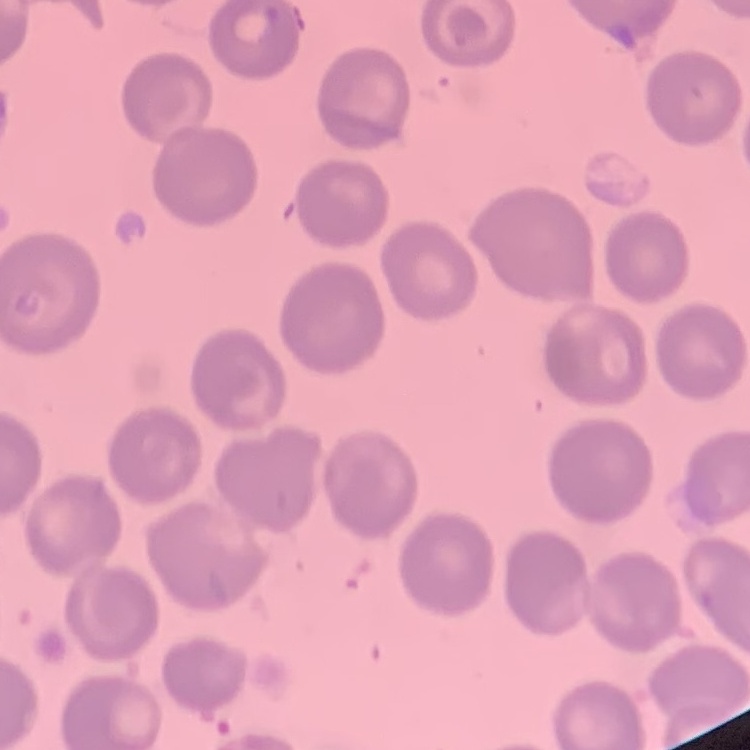
The erythrocytes show no rouleaux formation. Field's or Giemsa stain. One tile cut from a larger photomicrograph. Thin blood smear.